Assess this cell for malaria.
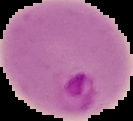

It is parasitized.

Summary:
  - Preparation: thin blood film
  - Image type: segmented cell region on a black background
  - Image size: 133×121 pixels